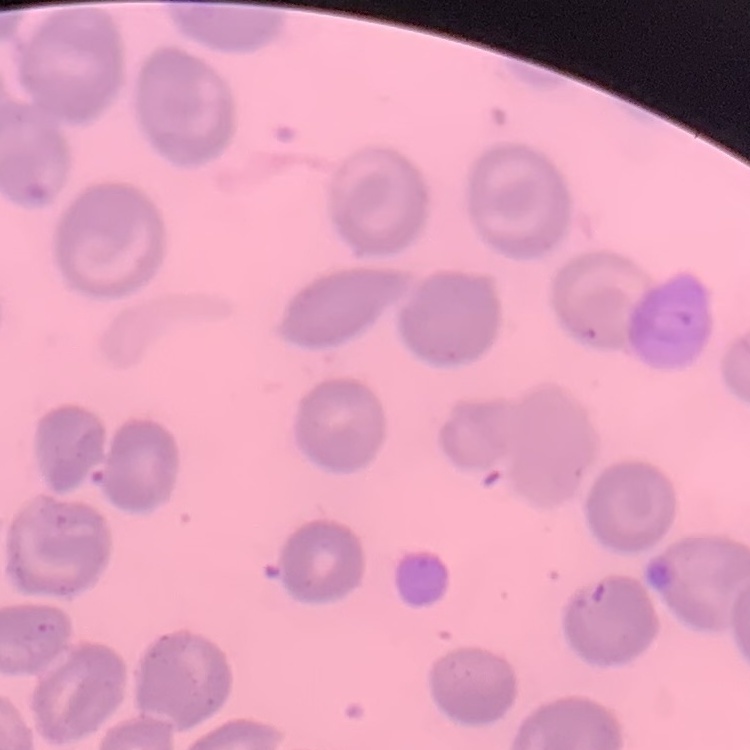
erythrocyte morphology = no rouleaux formation
preparation = thin blood smear
stain = Field's or Giemsa
image type = one tile cut from a larger photomicrograph